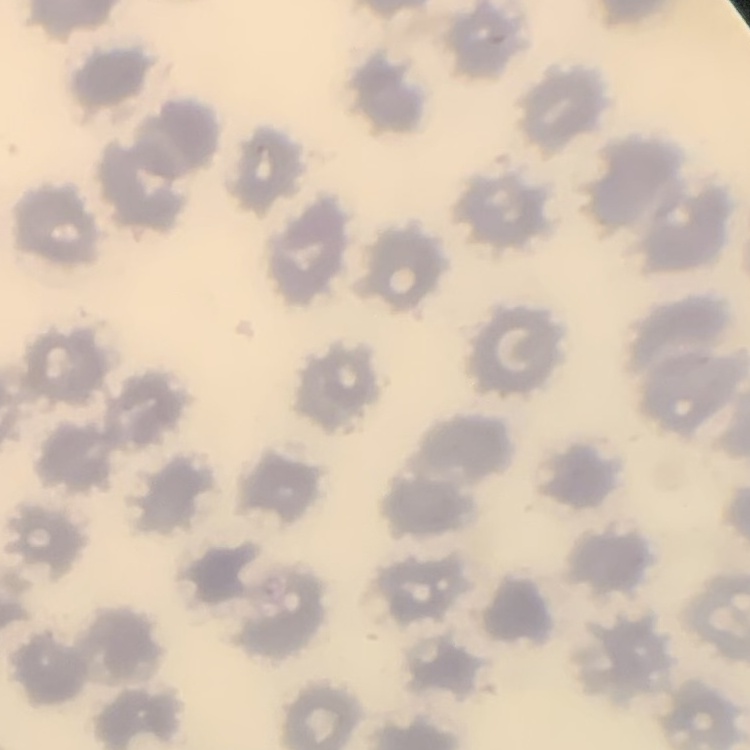
Summary:
  - Erythrocyte morphology: no rouleaux formation
  - Stain: Field's or Giemsa
  - Preparation: thin peripheral smear
  - Image type: one tile cut from a larger photomicrograph